Describe the morphology of the red blood cells.
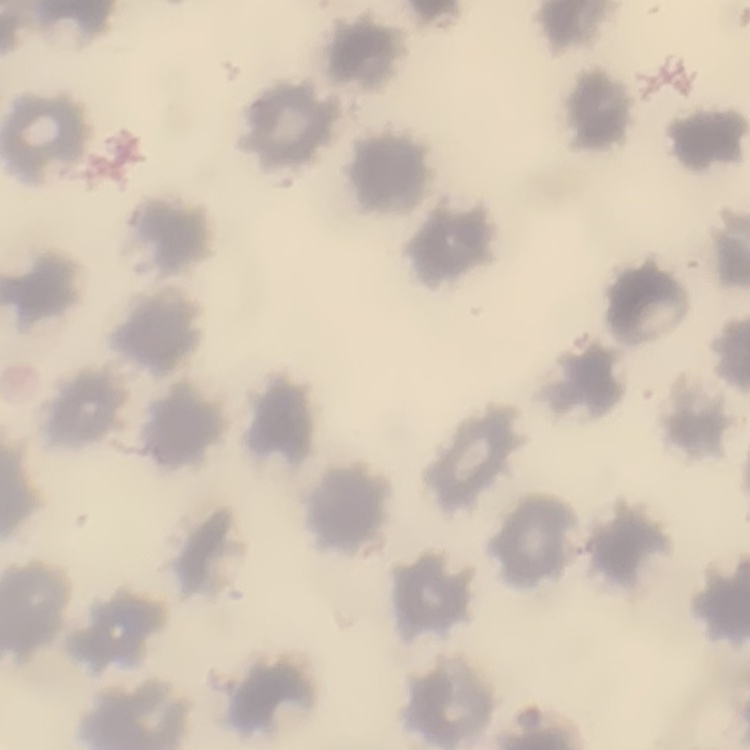

No rouleaux formation.

{
  "image_type": "one tile cut from a larger photomicrograph",
  "stain": "Field's or Giemsa",
  "preparation": "thin blood film"
}